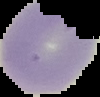 Result: no malaria parasites seen. Image is 100×97 pixels. From a thin blood smear. Segmented cell region on a black background.